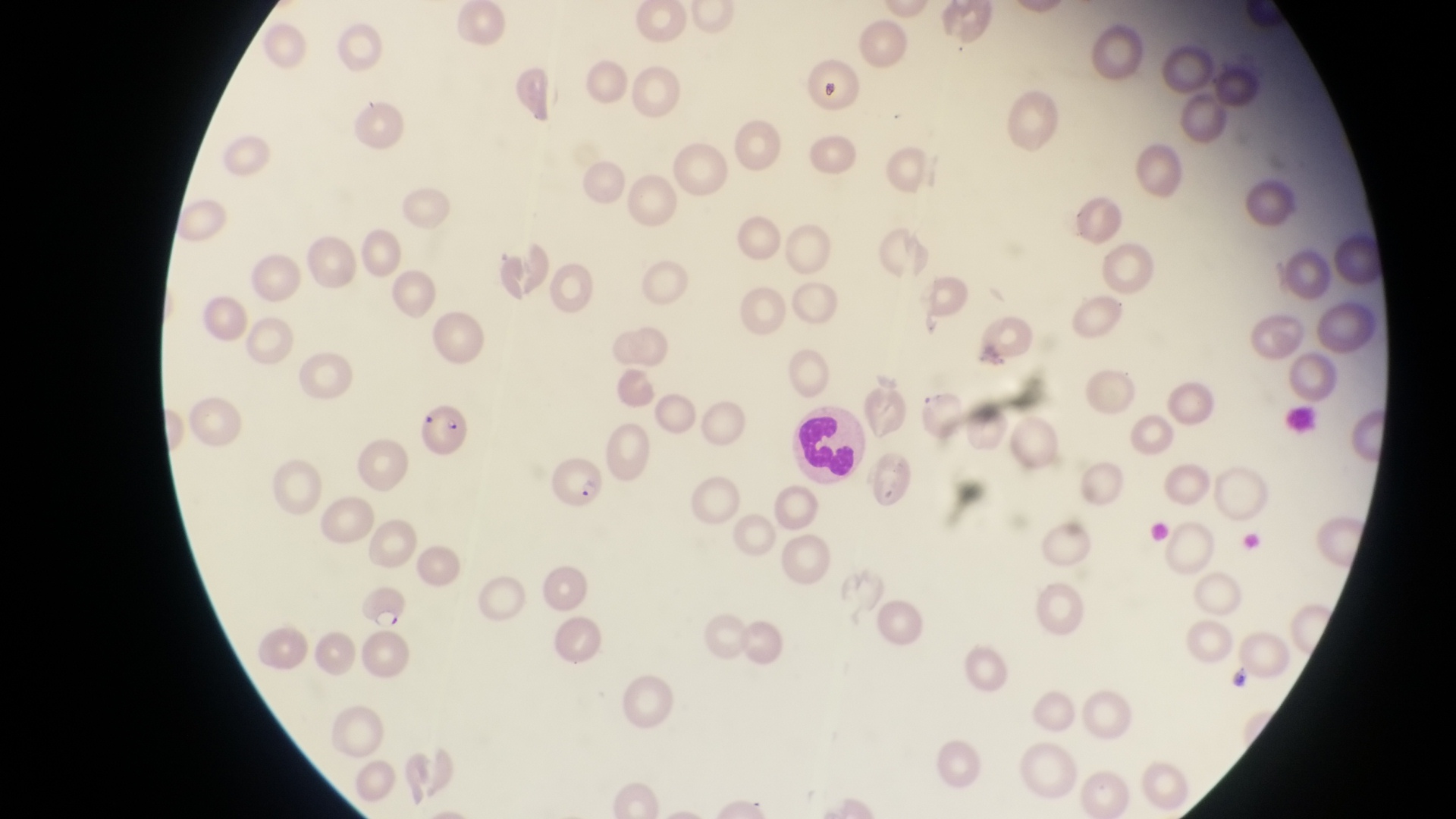

Approximate bounding boxes as {left, top, right, bottom} in pixels. Leukocyte locations: {798, 404, 867, 480}. Parasitised red blood cell locations: {419, 403, 469, 455}, {552, 457, 604, 510}, {349, 578, 409, 634}. Sample from Uganda. Thin blood smear. Magnification of 1000x. Image is 1456×819 pixels. Captured by a smartphone held over the eyepiece of an Olympus CX-23 microscope. Single field of view.